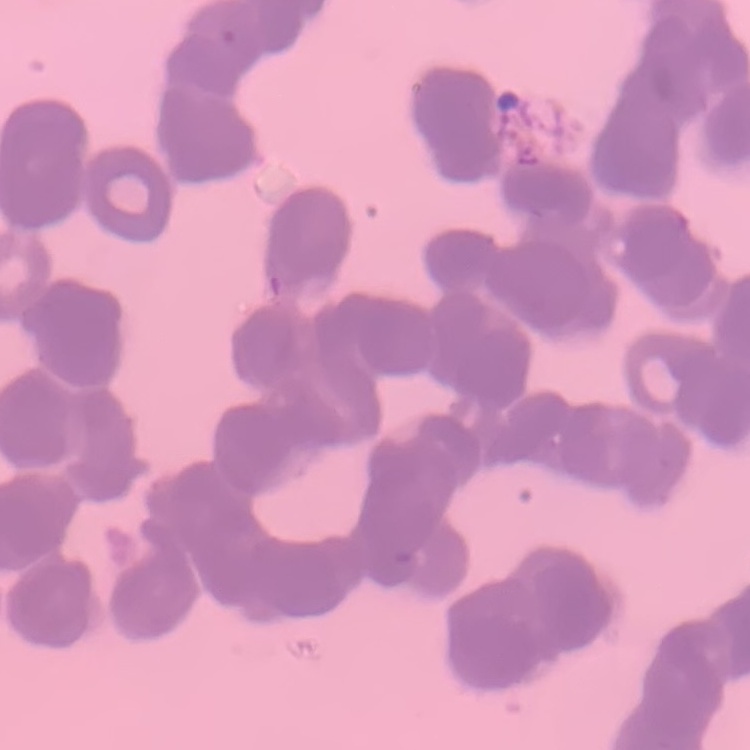
red blood cell morphology = rouleaux formation
stain = Field's or Giemsa
preparation = thin blood smear
image type = one tile cut from a larger photomicrograph